Identify the cell.
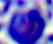

This is a leukocyte.

Summary:
  - Magnification: 400x
  - Modality: photomicrograph